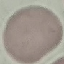

Summary:
  - Malaria status: uninfected
  - Preparation: thin blood film
  - Image type: cell patch, automatically extracted from a larger field of view and resized to 64 × 64 pixels
  - Capture: smartphone through the microscope eyepiece
  - Stain: Giemsa